Identify the preparation type.
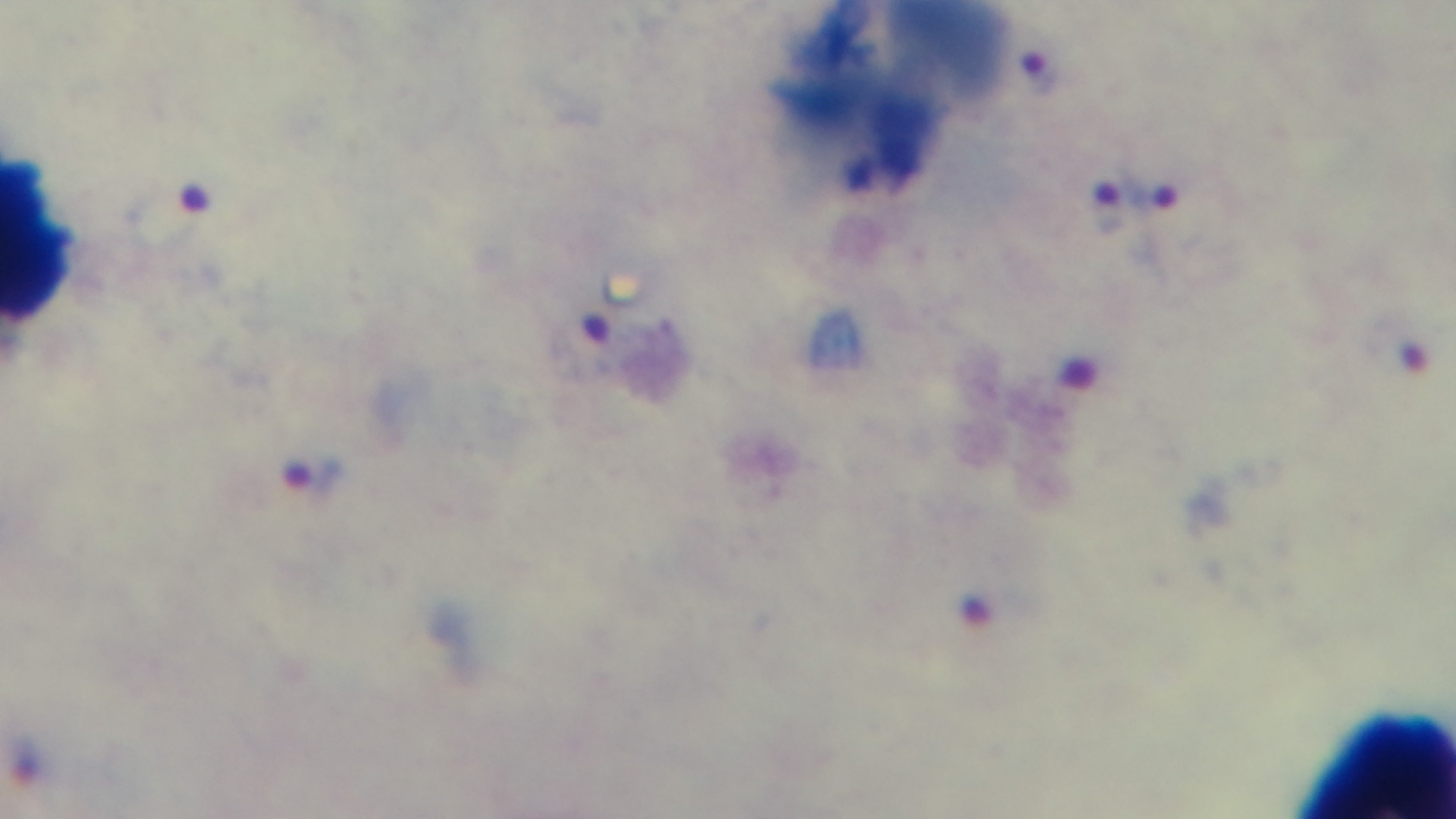
It is a thick blood film.

Summary:
  - Field of view: single
  - Capture: mounted 4K digital camera
  - Stain: Giemsa
  - Modality: light microscopy
  - Objective: 100x oil immersion
  - Malaria status: infected